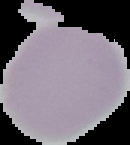
result: no malaria parasites seen
image_type: cell region segmented out of the field of view; surrounding area masked to black
preparation: thin blood smear
image_size: 130×145 pixels